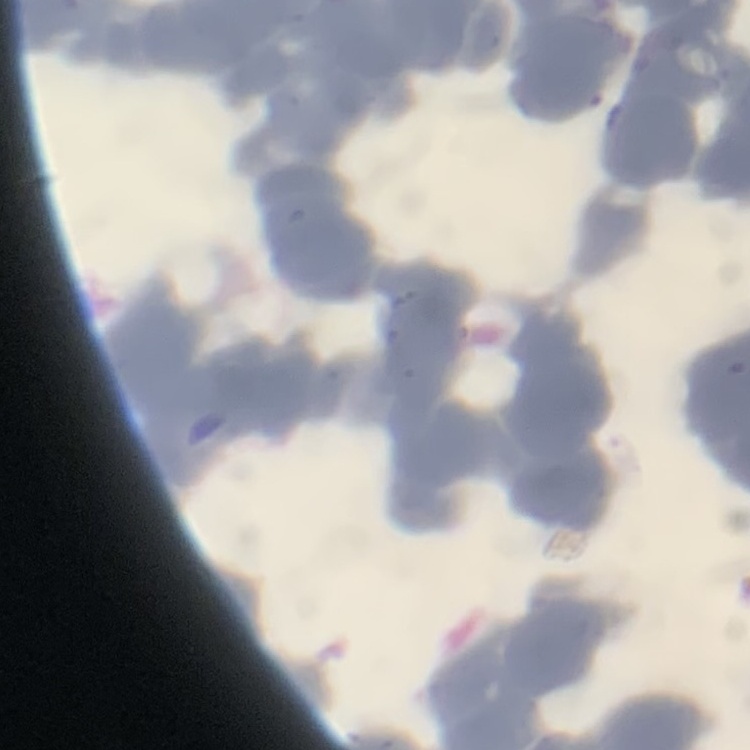
red_blood_cell_morphology: rouleaux formation
stain: Field's or Giemsa
preparation: thin peripheral smear
image_type: square crop of a larger photomicrograph